Identify the cell.
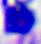

This is a leukocyte.

modality = photomicrograph
magnification = 400x